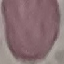

Summary:
  - Result: no malaria parasites detected
  - Image type: automatically extracted cell patch, resized to 64 × 64 pixels
  - Preparation: thin blood smear
  - Stain: Giemsa
  - Capture: smartphone through the microscope eyepiece